State which parasite is depicted.
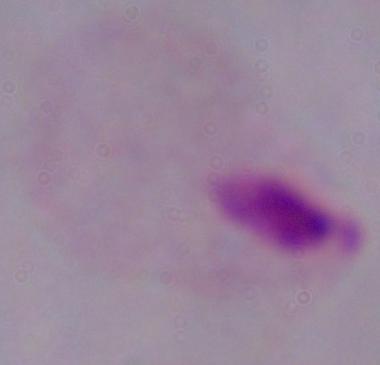

This is a trichomonad.

modality: photomicrograph
magnification: 1000x